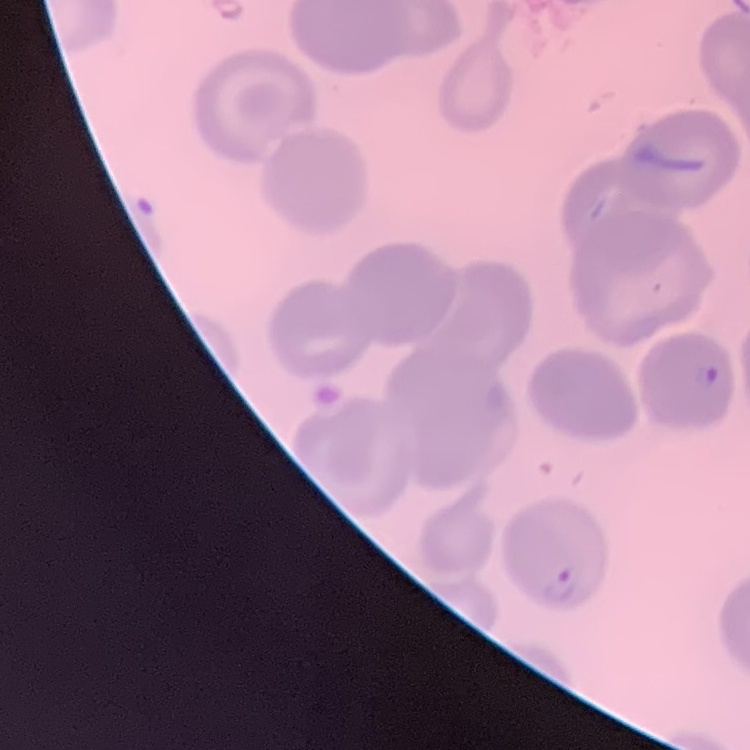
Summary:
  - Erythrocyte morphology: no rouleaux formation
  - Preparation: thin peripheral smear
  - Image type: one tile cut from a larger photomicrograph
  - Stain: Field's or Giemsa